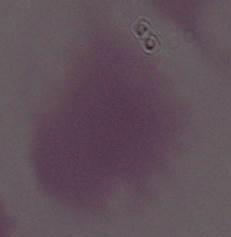

modality = micrograph
magnification = 1000x
identification = erythrocyte